Outline each Plasmodium falciparum-infected red blood cell.
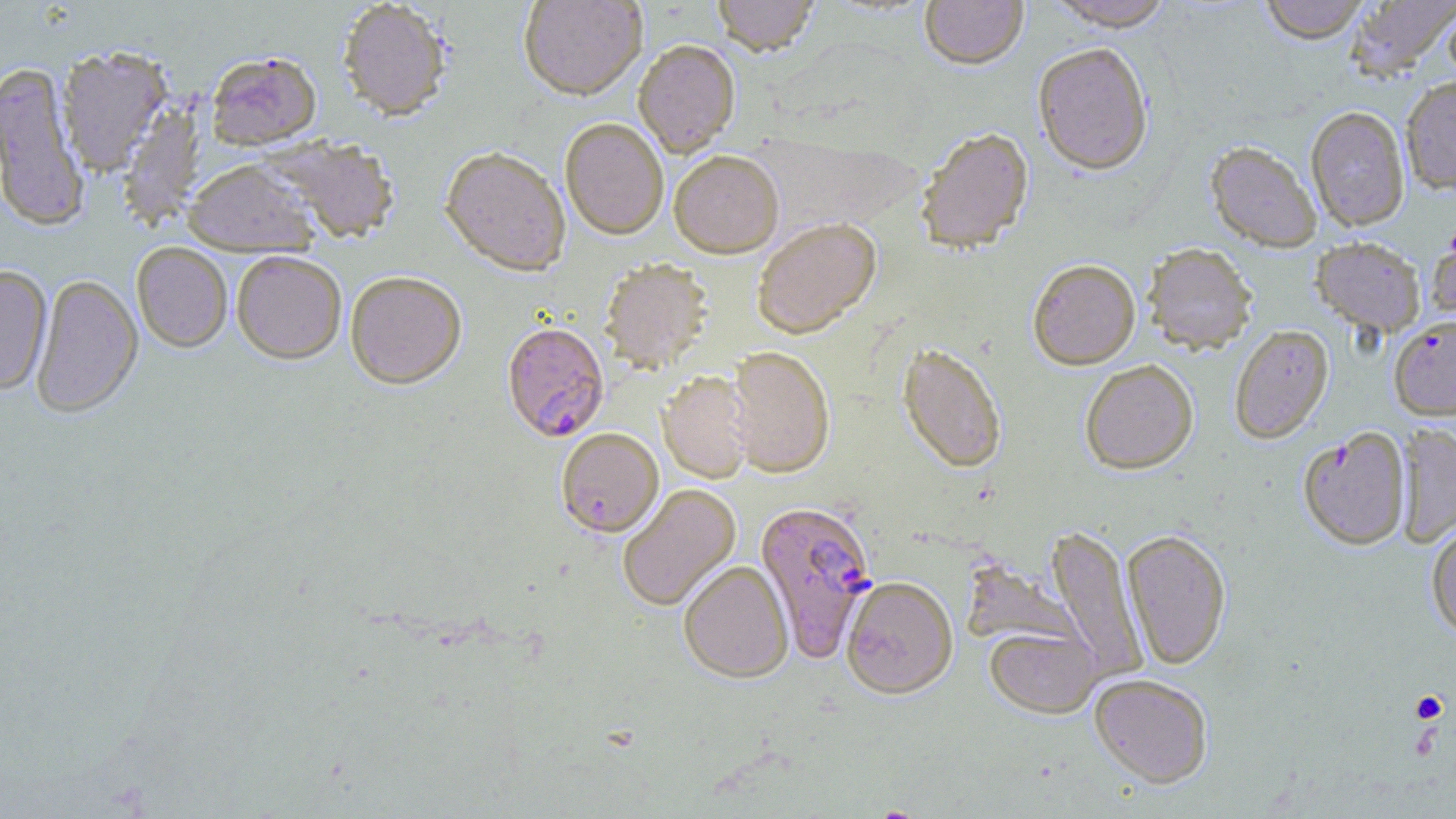
Approximate bounding boxes as (x1, y1, x2, y2) in pixels.
Plasmodium falciparum-infected red blood cells (subset): (502, 326, 609, 444), (1301, 425, 1414, 548), (754, 502, 877, 663).

Summary:
  - Platelet locations: (1410, 690, 1449, 723)
  - Uninfected red blood cell locations (subset): (518, 0, 647, 103), (712, 0, 819, 60), (920, 0, 1028, 71), (1045, 0, 1175, 31), (1258, 0, 1370, 44), (1345, 0, 1456, 80), (338, 3, 451, 124), (1442, 3, 1456, 91), (633, 42, 741, 159), (1033, 42, 1154, 177), (57, 47, 173, 175), (206, 55, 322, 153), (0, 61, 90, 233), (1400, 76, 1456, 194), (117, 102, 205, 232), (1306, 106, 1410, 231), (560, 120, 668, 242), (916, 129, 1035, 258), (259, 137, 399, 244), (1205, 143, 1321, 253), (440, 150, 571, 279), (669, 154, 784, 261), (183, 162, 319, 258), (753, 220, 882, 341), (1426, 223, 1456, 332), (1310, 236, 1426, 337), (131, 243, 232, 355), (1143, 245, 1257, 356), (231, 254, 346, 367), (600, 261, 714, 375), (1028, 262, 1140, 372), (0, 266, 52, 395), (345, 274, 467, 392), (31, 275, 144, 420), (1229, 325, 1333, 444), (897, 346, 1006, 475), (723, 349, 835, 480), (1080, 361, 1198, 475), (658, 373, 754, 485), (1394, 423, 1456, 548), (556, 430, 663, 539), (618, 484, 742, 612), (1426, 519, 1456, 640), (1046, 525, 1148, 681), (1121, 529, 1232, 670), (679, 563, 793, 685), (841, 579, 958, 702), (985, 627, 1102, 721), (1089, 674, 1214, 789)
  - Slide-level diagnosis: Plasmodium falciparum
  - Stain: May-Grünwald-Giemsa
  - Field of view: single
  - Preparation: thin blood film
  - Image size: 1456×819 pixels
  - Modality: optical microscopy
  - Magnification: 1000x